Find each white blood cell.
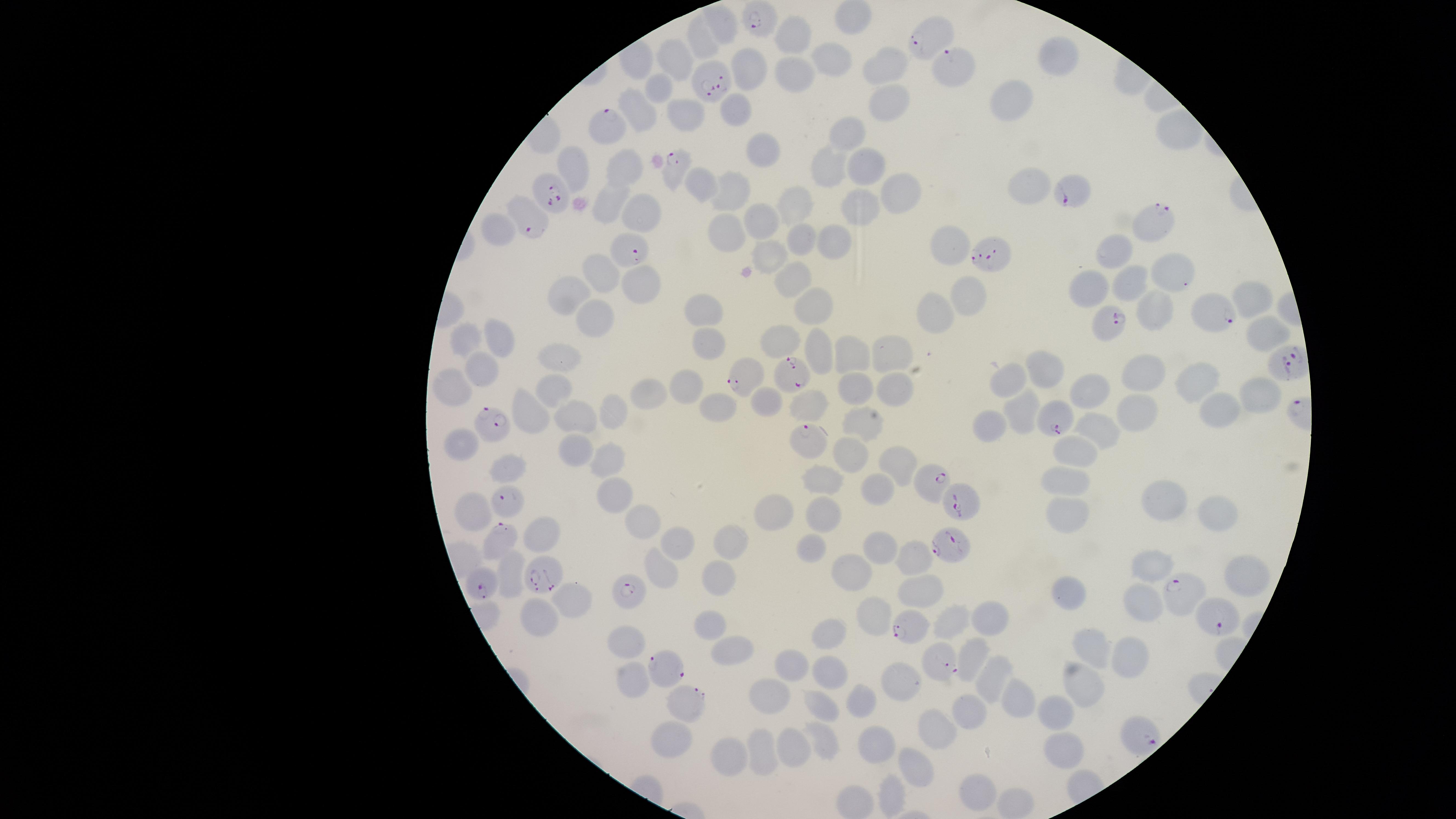

No white blood cells identified.

parasitized red blood cells = approximate marker points as [x, y] in pixels: [757, 21], [932, 38], [956, 66], [712, 78], [607, 127], [675, 169], [1075, 189], [554, 193], [1154, 219], [529, 222], [620, 248], [988, 254], [1213, 315], [1105, 327], [748, 373], [791, 376], [1057, 423], [501, 429], [805, 438], [932, 479], [961, 500], [508, 503], [500, 532], [949, 543], [546, 577], [482, 581], [628, 589], [1178, 595], [1222, 620], [905, 624], [673, 666], [946, 666], [683, 697], [1143, 732]
field of view = single
image size = 1456×819 pixels
visible region = circular
presence = malaria parasites identified
stain = Giemsa
uninfected red blood cells = approximate marker points as [x, y] in pixels: [721, 19], [794, 33], [702, 38], [1057, 53], [673, 56], [838, 62], [756, 65], [887, 68], [793, 69], [661, 84], [896, 96], [1020, 99], [734, 105], [642, 110], [685, 116], [851, 128], [761, 144], [837, 159], [623, 162], [570, 165], [866, 168], [1032, 182], [695, 185], [728, 189], [900, 189], [609, 197], [863, 202], [800, 203], [642, 211], [759, 220], [504, 230], [728, 230], [807, 239], [947, 242], [839, 243], [1115, 249], [773, 253], [600, 266], [1170, 267], [793, 277], [643, 281], [1132, 287], [1091, 288], [970, 289], [569, 292], [816, 302], [1249, 302], [705, 309], [1159, 312], [931, 314], [592, 316], [1265, 330], [468, 333], [497, 334], [775, 338], [713, 345], [816, 352], [897, 352], [849, 355], [562, 357], [1048, 370], [486, 371], [1016, 376], [1152, 380], [552, 381], [1199, 382], [687, 383], [858, 384], [1091, 388], [452, 389], [898, 391], [1261, 391], [647, 393], [715, 404], [810, 404], [770, 406], [526, 407], [1223, 408], [613, 410], [1024, 412], [579, 415], [1134, 415], [857, 419], [1097, 425], [988, 426], [462, 441], [574, 446], [1076, 451], [854, 454], [603, 460], [901, 464], [512, 471], [1068, 478], [829, 480], [879, 494], [619, 495], [1168, 497], [1217, 507], [777, 509], [472, 510], [826, 515], [1066, 515], [648, 516], [546, 536], [680, 539], [883, 542], [813, 543], [725, 544], [916, 555], [513, 563], [656, 563], [1156, 563], [841, 565], [1243, 575], [718, 576], [920, 585], [1066, 591], [570, 595], [1141, 601], [884, 610], [992, 616], [535, 617], [948, 622], [708, 623], [828, 631], [629, 638], [726, 645], [977, 648], [1091, 651], [1135, 654], [791, 663], [829, 672], [1080, 677], [634, 678], [988, 680], [896, 693], [769, 695], [860, 700], [1016, 703], [822, 706], [1056, 708], [971, 714], [937, 727], [666, 734], [821, 738], [787, 743], [878, 748], [760, 749], [1067, 753], [732, 755], [913, 765], [982, 787], [890, 797]
preparation = thin smear of blood
capture = smartphone photograph through the microscope eyepiece
species = Plasmodium falciparum